Outline each uninfected red blood cell.
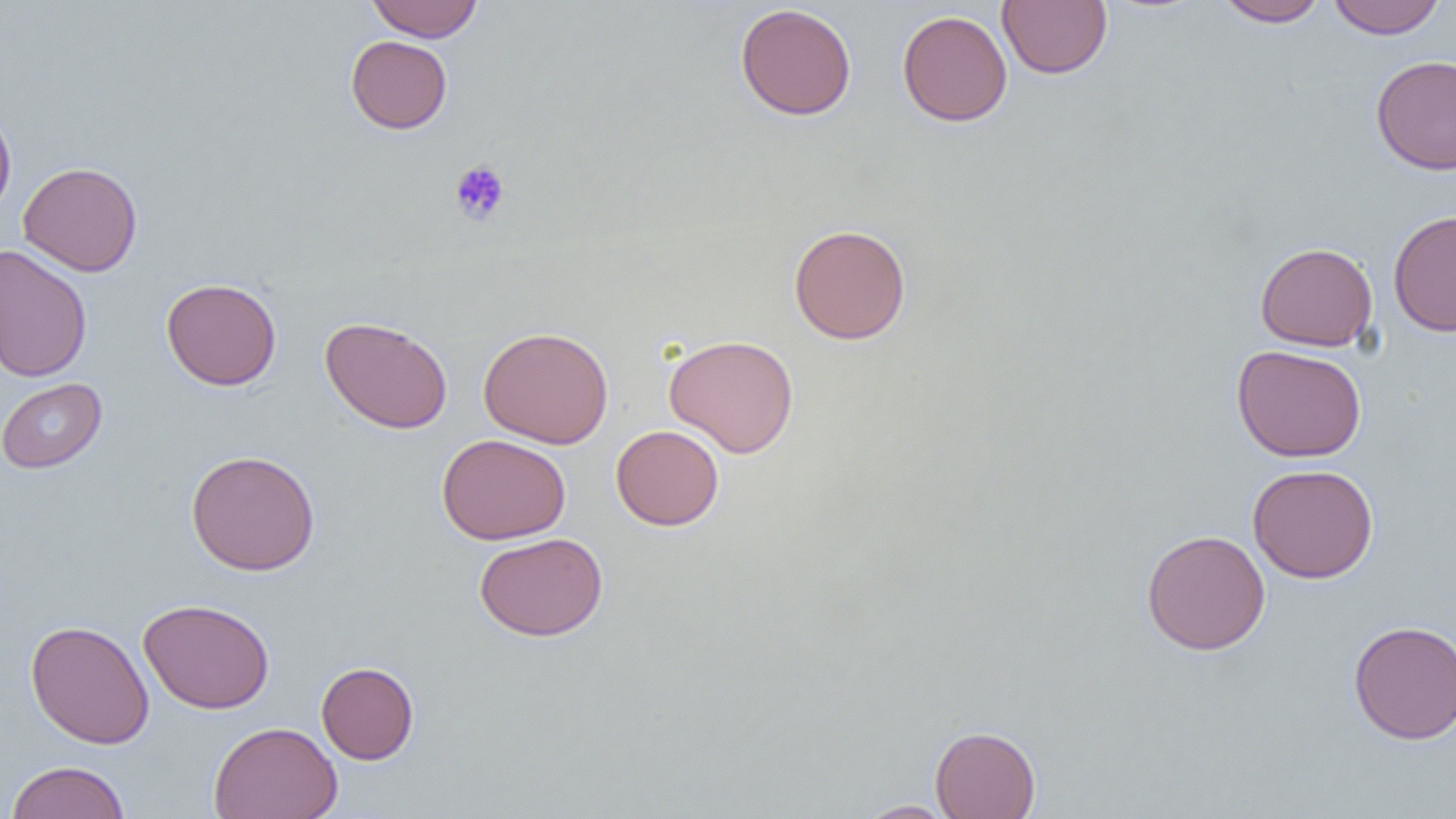

Approximate bounding boxes as (x1,y1)-(x2,y2) corner pairs in pixels.
Uninfected red blood cells: (366,0)-(483,42), (997,0)-(1112,79), (1214,0)-(1329,27), (1327,0)-(1447,39), (735,3)-(858,121), (897,9)-(1012,126), (346,35)-(452,134), (1370,53)-(1456,175), (0,106)-(17,221), (18,161)-(144,277), (1388,209)-(1456,336), (788,223)-(911,344), (1254,241)-(1378,351), (0,244)-(92,383), (161,278)-(281,391), (319,316)-(453,434), (478,326)-(614,449), (663,334)-(799,458), (1231,343)-(1367,462), (0,378)-(107,473), (611,424)-(725,531), (437,433)-(571,544), (186,450)-(320,576), (1247,463)-(1379,583), (1141,529)-(1271,655), (474,532)-(608,641), (138,598)-(275,714), (26,619)-(154,749), (1348,620)-(1456,745), (316,661)-(419,765), (208,721)-(343,819), (930,726)-(1041,819), (5,760)-(131,819), (856,800)-(958,818).

Platelet locations: (449,159)-(511,226). Slide-level diagnosis: no evidence of blood parasites. Captured at 1000x magnification. Image is 1456×819 pixels. Thin blood smear. Light microscopy. One field of a larger specimen.